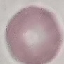
Summary:
  - Malaria status: uninfected
  - Image type: cell patch, automatically extracted from a larger field of view and resized to 64 × 64 pixels
  - Preparation: thin blood smear
  - Stain: Giemsa
  - Capture: smartphone through the microscope eyepiece